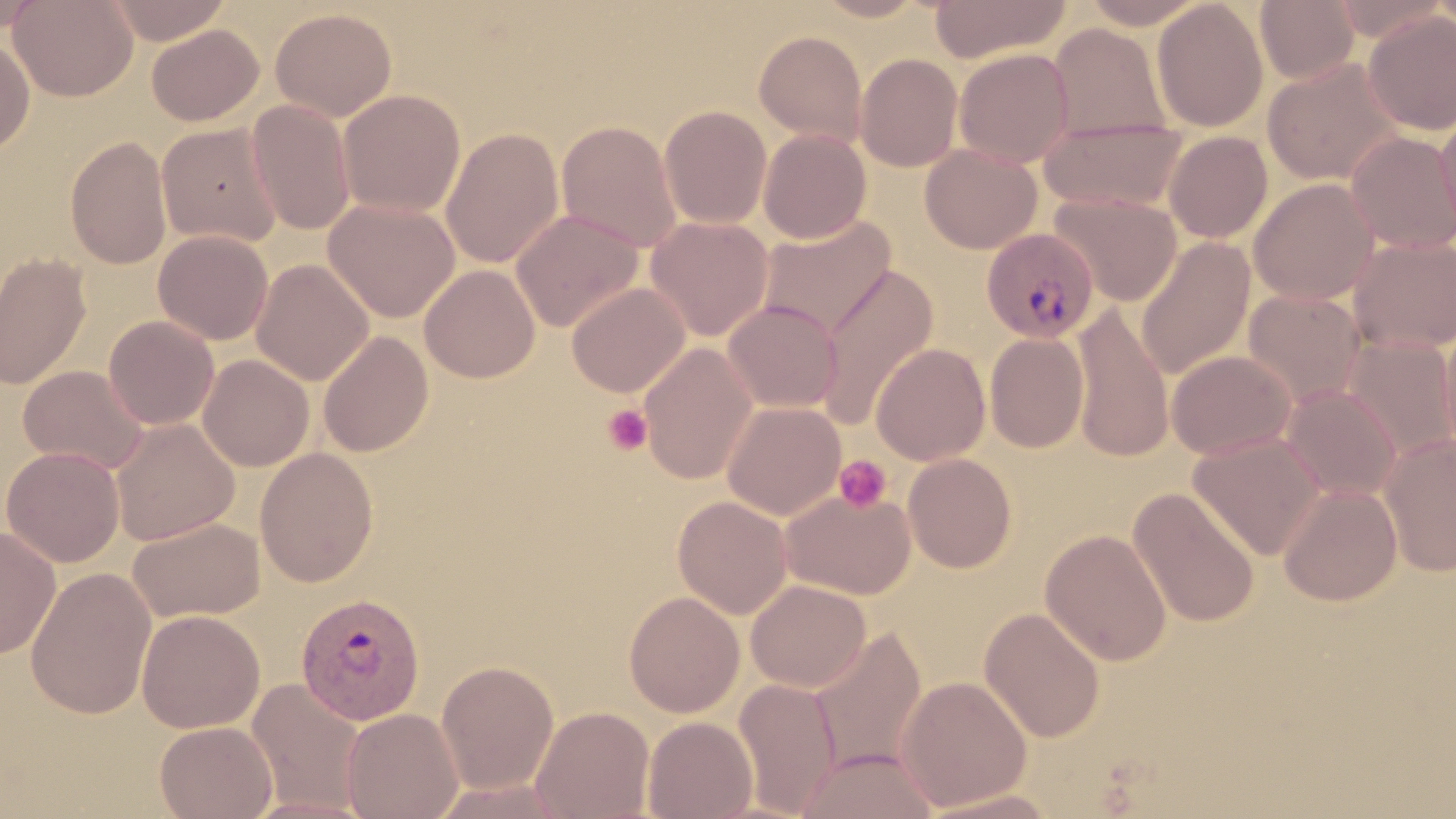 Approximate bounding boxes as [x1, y1, x2, y2] in pixels. Plasmodium vivax-infected red blood cell locations: [979, 226, 1098, 341], [296, 591, 426, 726]. Platelet locations: [602, 403, 653, 456], [834, 454, 893, 513]. Uninfected red blood cell locations: [8, 0, 138, 102], [103, 0, 233, 45], [811, 0, 931, 22], [928, 0, 1071, 64], [1079, 0, 1209, 29], [1151, 0, 1268, 132], [1255, 0, 1359, 85], [0, 2, 44, 35], [270, 8, 397, 122], [1362, 11, 1456, 135], [1048, 23, 1171, 142], [146, 24, 263, 126], [753, 30, 867, 145], [0, 34, 35, 156], [759, 41, 970, 154], [954, 48, 1075, 167], [855, 53, 963, 172], [1262, 58, 1404, 186], [338, 89, 466, 218], [246, 100, 356, 235], [1435, 103, 1456, 239], [659, 105, 773, 229], [1039, 118, 1190, 212], [556, 120, 683, 253], [156, 123, 284, 248], [440, 127, 565, 269], [758, 129, 871, 244], [1163, 130, 1273, 243], [1346, 131, 1456, 253], [65, 135, 172, 270], [920, 144, 1042, 254], [1248, 178, 1380, 305], [1050, 193, 1182, 306], [324, 197, 460, 323], [511, 209, 644, 333], [646, 215, 774, 342], [757, 215, 896, 341], [153, 229, 274, 345], [1347, 235, 1456, 354], [1136, 238, 1255, 380], [0, 251, 92, 390], [250, 259, 374, 385], [419, 263, 541, 382], [816, 264, 939, 431], [567, 281, 690, 397], [1243, 289, 1366, 408], [723, 300, 842, 413], [1070, 303, 1174, 461], [103, 315, 219, 430], [1439, 316, 1456, 461], [318, 331, 434, 458], [985, 333, 1089, 453], [1342, 335, 1456, 461], [638, 342, 759, 485], [870, 343, 990, 466], [1166, 349, 1296, 460], [198, 354, 314, 472], [18, 364, 149, 474], [1282, 385, 1401, 502], [722, 400, 846, 520], [110, 417, 240, 546], [1378, 432, 1456, 577], [1188, 433, 1326, 560], [1, 446, 125, 567], [254, 447, 379, 588], [902, 453, 1017, 573], [1278, 482, 1403, 606], [779, 487, 917, 600], [1127, 487, 1261, 628], [672, 495, 793, 619], [126, 517, 265, 623], [0, 526, 61, 660], [1040, 528, 1173, 666], [25, 567, 157, 719], [745, 579, 871, 692], [623, 590, 745, 717], [979, 607, 1106, 743], [137, 609, 264, 733], [808, 628, 927, 778], [435, 659, 560, 794], [897, 675, 1033, 810], [733, 676, 842, 817], [246, 677, 368, 814], [531, 705, 655, 819], [341, 707, 465, 819], [642, 715, 757, 819], [154, 721, 277, 819], [795, 747, 940, 819], [428, 778, 579, 818], [916, 788, 1066, 818], [238, 794, 380, 819]. Slide-level diagnosis: Plasmodium vivax. Thin blood smear. Light microscopy. Image is 1456×819 pixels. Single field of view. May-Grünwald-Giemsa stain. Captured at 1000x magnification.